Classify this cell by malaria status.
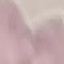

Uninfected.

preparation = thin blood smear
image type = cell patch, automatically extracted from a larger field of view and resized to 64 × 64 pixels
stain = Giemsa
capture = smartphone through the microscope eyepiece